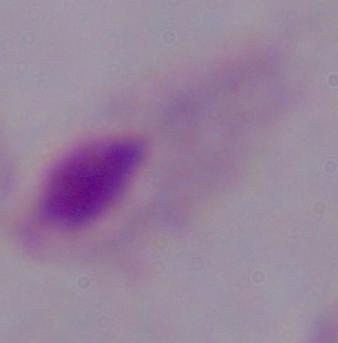

A trichomonad is seen. 1000x magnification. Photomicrograph.